Name the parasite shown.
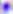
Toxoplasma gondii.

Summary:
  - Magnification: 400x
  - Modality: photomicrograph